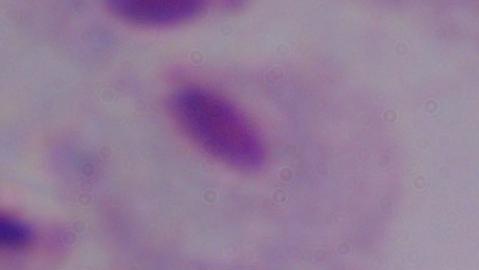 Captured at 1000x magnification. A trichomonad is shown. Photomicrograph.